State which parasite is depicted.
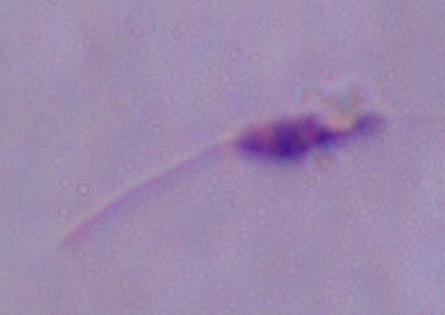
This is Leishmania.

{
  "magnification": "1000x",
  "modality": "photomicrograph"
}